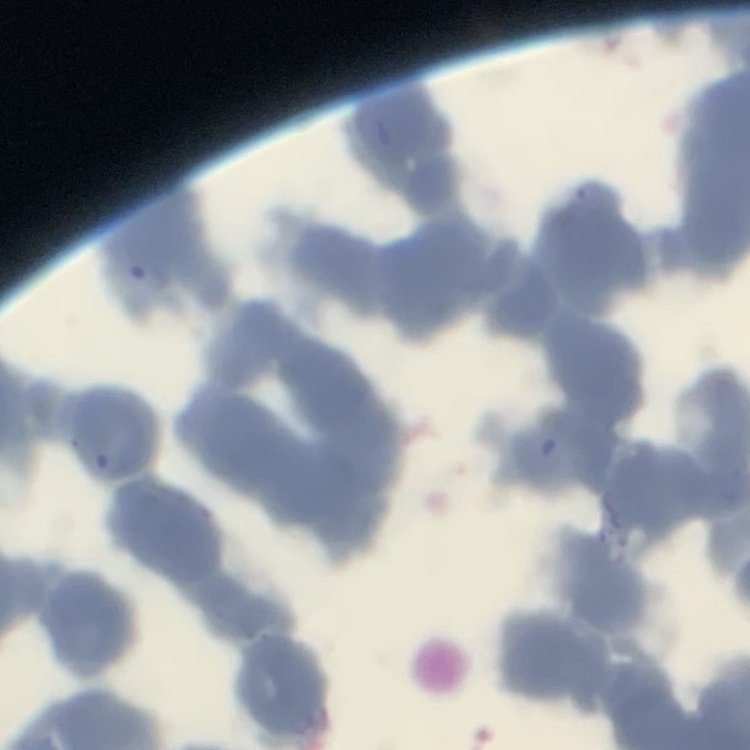

red_blood_cell_morphology: rouleaux formation
stain: Field's or Giemsa
image_type: square crop of a larger photomicrograph
preparation: thin blood smear